Assess the morphology of the red blood cells.
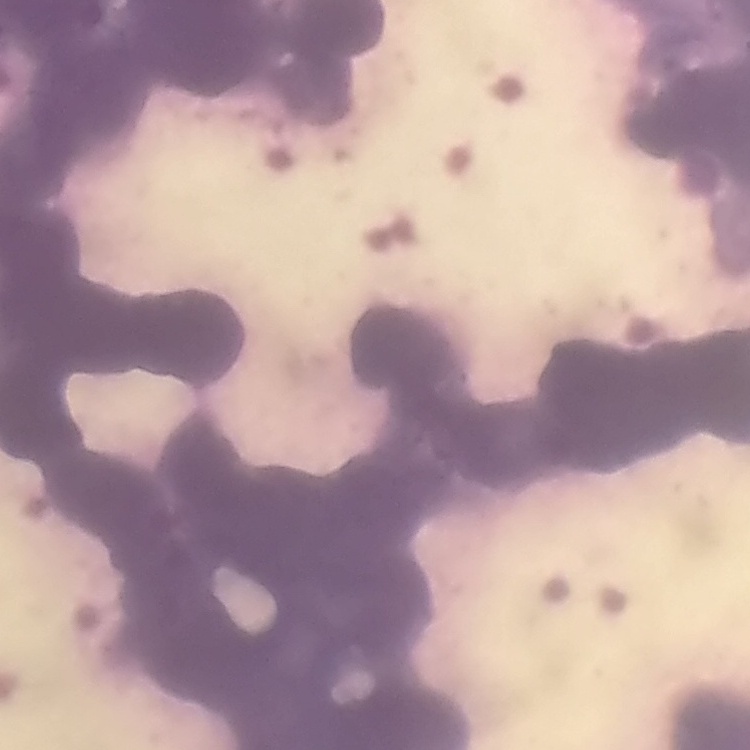
Rouleaux formation.

stain = Field's or Giemsa
image type = one tile cut from a larger photomicrograph
preparation = thin peripheral smear